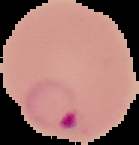

Summary:
  - Image size: 139×145 pixels
  - Malaria status: parasitized
  - Preparation: thin blood film
  - Image type: cell region segmented out of the field of view; surrounding area masked to black